Locate every Plasmodium falciparum-infected red blood cell.
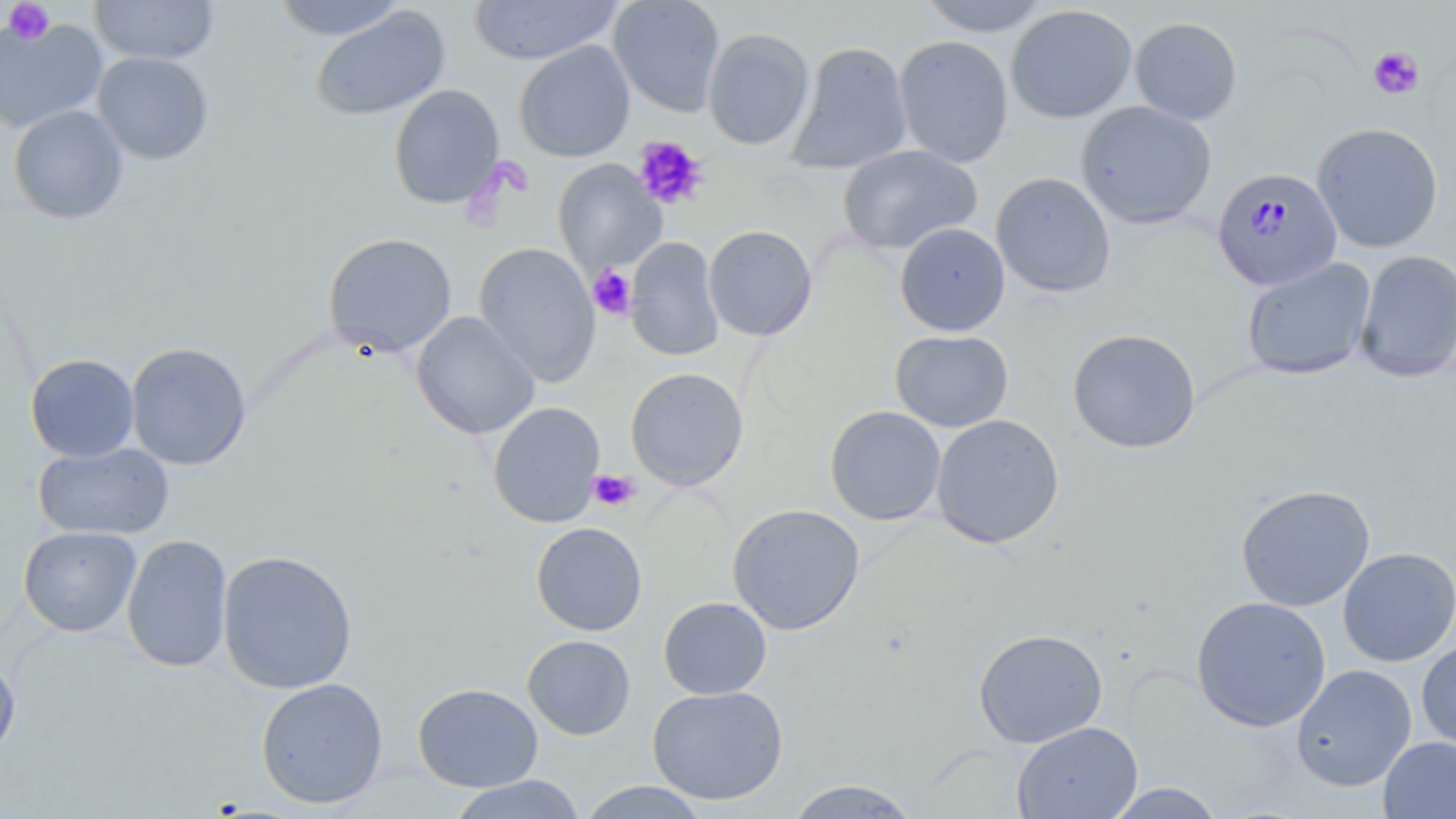
Approximate bounding boxes as [x1, y1, x2, y2] in pixels.
Plasmodium falciparum-infected red blood cells: [1212, 166, 1343, 292].

slide-level diagnosis = Plasmodium falciparum
stain = May-Grünwald-Giemsa
modality = optical microscopy
preparation = thin blood smear
image size = 1456×819 pixels
field of view = single
magnification = 1000x
platelet locations = approximate bounding boxes as [x1, y1, x2, y2] in pixels: [4, 1, 54, 45], [1368, 46, 1424, 100], [633, 136, 709, 210], [588, 266, 636, 319], [588, 470, 640, 512]
uninfected red blood cell locations = approximate bounding boxes as [x1, y1, x2, y2] in pixels: [88, 0, 220, 66], [271, 0, 407, 41], [468, 0, 624, 65], [609, 0, 725, 117], [918, 0, 1053, 36], [1005, 4, 1138, 124], [311, 6, 450, 121], [0, 15, 107, 134], [1130, 17, 1243, 125], [702, 28, 814, 151], [894, 35, 1014, 168], [514, 41, 635, 162], [786, 41, 912, 175], [93, 51, 213, 165], [388, 84, 505, 210], [1076, 101, 1217, 230], [8, 104, 129, 224], [1312, 122, 1444, 252], [838, 145, 983, 255], [554, 159, 666, 275], [991, 171, 1115, 298], [895, 223, 1010, 337], [703, 225, 818, 341], [322, 232, 457, 358], [626, 237, 724, 362], [474, 242, 601, 387], [1354, 249, 1456, 383], [1242, 257, 1376, 380], [411, 311, 540, 439], [1067, 328, 1201, 454], [890, 329, 1013, 432], [126, 341, 251, 470], [25, 353, 139, 462], [625, 367, 749, 491], [488, 402, 605, 528], [825, 405, 946, 525], [930, 413, 1065, 549], [32, 442, 175, 540], [1235, 484, 1375, 612], [728, 503, 865, 636], [531, 521, 647, 636], [18, 525, 141, 636], [121, 533, 233, 673], [1339, 547, 1456, 667], [217, 550, 358, 694], [1191, 595, 1331, 732], [658, 596, 772, 700], [973, 628, 1108, 748], [522, 634, 635, 740], [1416, 639, 1456, 753], [0, 657, 21, 762], [1291, 664, 1417, 792], [255, 677, 389, 808], [413, 682, 543, 791], [647, 685, 788, 805], [1012, 721, 1143, 819], [1378, 736, 1456, 818], [447, 775, 587, 819], [783, 779, 923, 818], [576, 781, 712, 818], [1103, 783, 1227, 818]